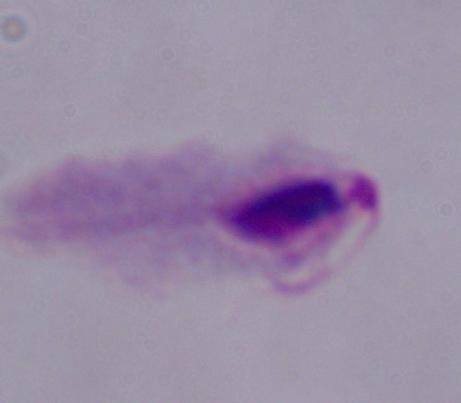

1000x magnification. Photomicrograph. A trichomonad is shown.